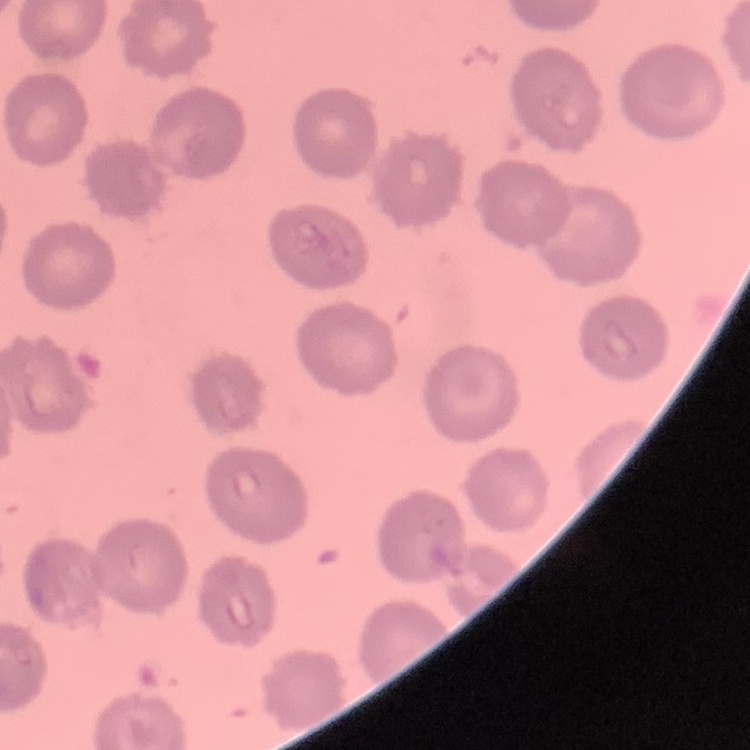
erythrocyte morphology = no rouleaux formation
preparation = thin blood film
stain = Field's or Giemsa
image type = one tile cut from a larger photomicrograph